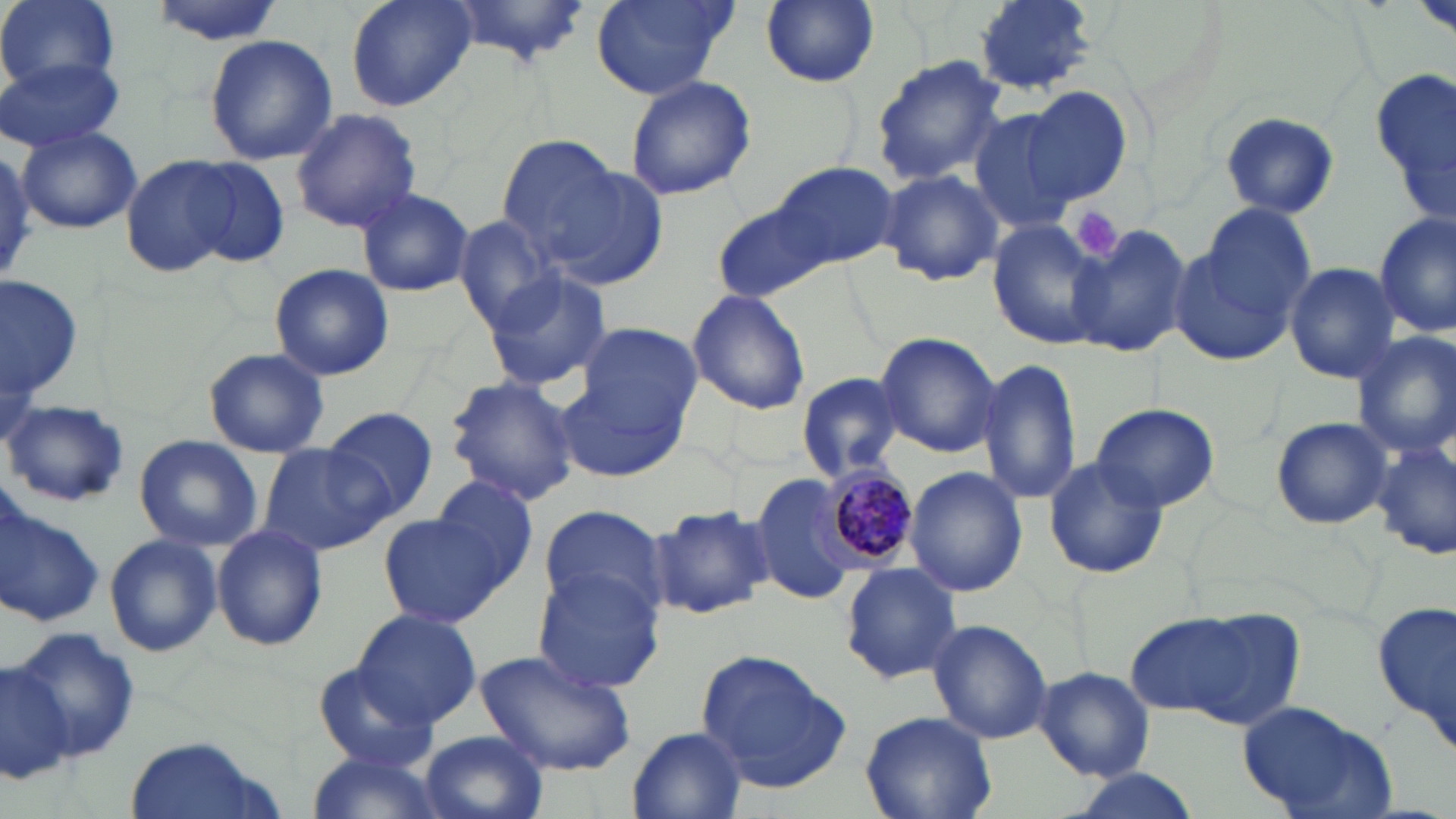
Approximate bounding boxes as (x1, y1, x2, y2) in pixels. Plasmodium malariae-infected red blood cell locations: (823, 463, 919, 566). Uninfected red blood cell locations: (2, 0, 119, 94), (146, 0, 287, 44), (342, 0, 477, 113), (591, 0, 735, 100), (760, 0, 880, 88), (973, 0, 1098, 94), (443, 1, 593, 67), (1413, 2, 1455, 37), (204, 34, 336, 166), (0, 55, 125, 153), (869, 55, 1008, 184), (1370, 70, 1456, 217), (624, 72, 756, 201), (1021, 85, 1134, 205), (289, 106, 422, 233), (969, 108, 1080, 236), (1220, 112, 1340, 218), (17, 129, 142, 234), (492, 134, 636, 266), (0, 145, 35, 286), (120, 154, 243, 279), (179, 155, 292, 269), (770, 160, 895, 271), (537, 162, 670, 292), (876, 169, 1004, 286), (355, 186, 475, 297), (719, 203, 833, 304), (1374, 211, 1454, 338), (454, 215, 561, 332), (986, 221, 1106, 349), (1069, 224, 1192, 359), (1170, 224, 1307, 366), (1284, 261, 1401, 385), (268, 263, 395, 382), (482, 269, 614, 392), (2, 277, 84, 414), (687, 288, 811, 415), (579, 323, 703, 431), (1352, 330, 1456, 459), (874, 332, 1001, 457), (203, 347, 329, 458), (977, 357, 1084, 508), (556, 371, 690, 483), (797, 371, 904, 481), (443, 375, 582, 505), (5, 399, 130, 509), (1092, 403, 1221, 512), (322, 406, 439, 520), (1270, 416, 1391, 529), (133, 435, 263, 551), (1372, 439, 1454, 560), (258, 444, 393, 556), (1042, 457, 1170, 578), (905, 466, 1027, 598), (429, 474, 541, 588), (751, 475, 865, 604), (0, 493, 104, 629), (650, 501, 776, 619), (537, 505, 669, 622), (378, 512, 509, 628), (211, 524, 328, 651), (104, 532, 222, 658), (839, 562, 962, 683), (533, 569, 665, 695), (1371, 598, 1456, 753), (1130, 603, 1305, 730), (351, 608, 481, 727), (928, 618, 1052, 746), (10, 626, 142, 763), (473, 650, 637, 776), (695, 650, 851, 792), (0, 656, 74, 787), (311, 662, 438, 772), (1035, 666, 1155, 780), (1236, 700, 1400, 818), (862, 710, 997, 818), (628, 727, 748, 817), (419, 729, 548, 819), (124, 736, 273, 819), (302, 750, 446, 819), (1067, 769, 1203, 819). Platelet locations: (1071, 207, 1125, 259). Slide-level diagnosis: Plasmodium malariae. Image is 1456×819 pixels. One field of a larger specimen. May-Grünwald-Giemsa stain. 1000x magnification. Thin blood film. Optical microscopy.